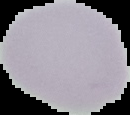 The area outside the segmented cell region is set to black. Image is 130×115 pixels. From a thin blood film. Malaria status: uninfected.